Describe the morphology of the red blood cells.
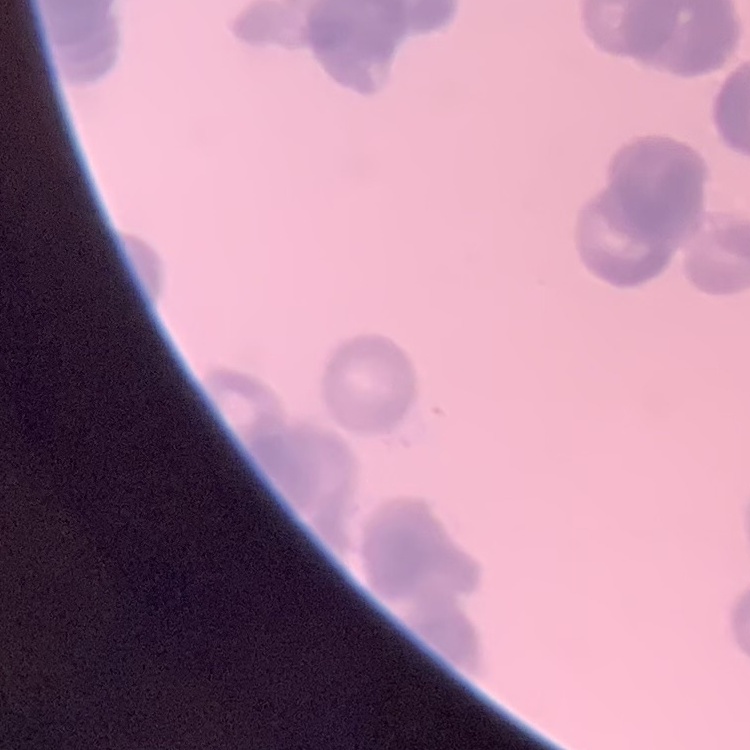

They show rouleaux formation.

Square crop of a larger photomicrograph. Thin blood smear. Stained with either Field's or Giemsa.